Identify the parasite.
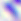
This is Toxoplasma gondii.

modality = photomicrograph
magnification = 400x